Locate and identify every blood parasite.
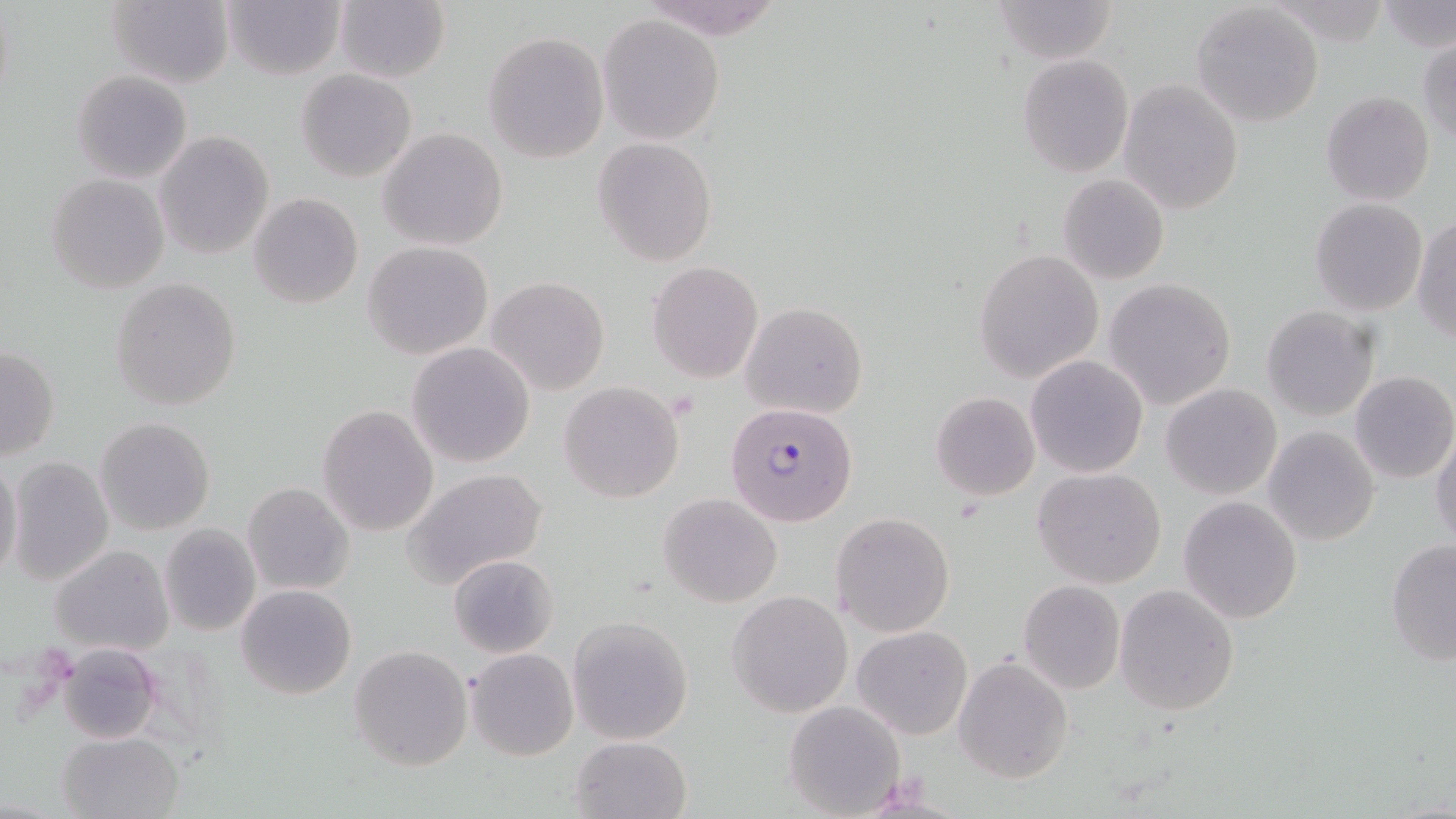
Approximate bounding boxes as (x1, y1, x2, y2) in pixels.
Plasmodium falciparum-infected red blood cells: (724, 402, 857, 527).
No Plasmodium ovale, Plasmodium malariae, Plasmodium vivax, Babesia divergens, or Trypanosoma brucei observed.

Uninfected red blood cell locations: (107, 0, 235, 89), (336, 0, 450, 83), (989, 0, 1120, 65), (221, 1, 344, 80), (1259, 1, 1395, 44), (1381, 2, 1456, 52), (1191, 3, 1325, 127), (597, 14, 725, 145), (483, 32, 610, 162), (1417, 36, 1456, 144), (1017, 56, 1133, 177), (297, 70, 416, 182), (71, 71, 192, 182), (1120, 79, 1243, 214), (1321, 92, 1434, 205), (379, 128, 509, 249), (153, 132, 274, 258), (593, 137, 716, 266), (47, 173, 168, 294), (1057, 174, 1168, 284), (248, 192, 363, 309), (1309, 198, 1428, 316), (1413, 214, 1456, 343), (363, 242, 494, 360), (974, 249, 1103, 383), (646, 261, 763, 383), (487, 276, 610, 395), (1103, 278, 1237, 409), (110, 279, 242, 410), (742, 301, 868, 418), (1262, 306, 1379, 420), (406, 342, 536, 467), (0, 346, 60, 461), (1026, 356, 1147, 477), (1350, 371, 1456, 484), (558, 381, 685, 502), (1160, 384, 1282, 500), (931, 392, 1040, 501), (317, 405, 438, 538), (95, 417, 215, 534), (1264, 426, 1379, 546), (1431, 428, 1456, 553), (7, 456, 114, 587), (0, 458, 24, 583), (404, 468, 550, 591), (1033, 468, 1166, 588), (242, 482, 355, 597), (658, 493, 782, 607), (1178, 496, 1303, 623), (831, 512, 955, 637), (158, 524, 261, 637), (1385, 537, 1456, 668), (49, 544, 174, 657), (448, 554, 558, 657), (1016, 581, 1125, 695), (236, 585, 357, 699), (1115, 585, 1239, 716), (728, 590, 852, 716), (567, 616, 694, 743), (852, 625, 973, 739), (60, 641, 161, 744), (350, 645, 472, 770), (467, 648, 577, 760), (954, 655, 1072, 784), (783, 700, 906, 817), (58, 731, 183, 819), (570, 735, 693, 819). Slide-level diagnosis: Plasmodium falciparum. Optical microscopy. Single field of view. May-Grünwald-Giemsa stain. Thin blood smear. Image is 1456×819 pixels. 1000x magnification.